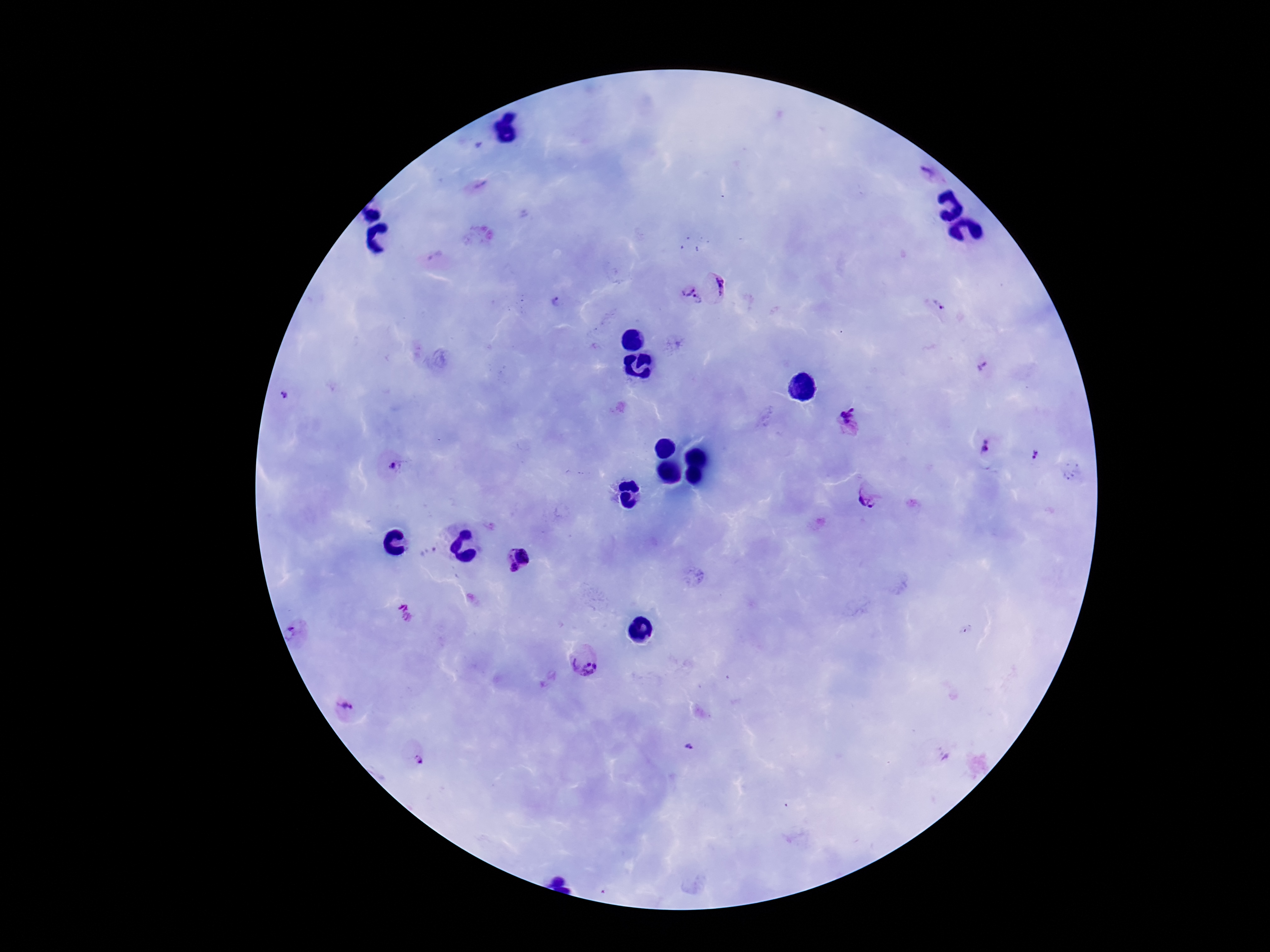
magnification = 100x
image size = 1270×952 pixels
capture = smartphone camera through the microscope eyepiece
preparation = thick peripheral-blood smear
field of view = one from this slide
Plasmodium parasite locations = approximate object centers, in pixels from the top-left corner: (x=928, y=173), (x=476, y=188), (x=717, y=286), (x=691, y=298), (x=555, y=302), (x=938, y=305), (x=983, y=367), (x=284, y=395), (x=850, y=423), (x=986, y=445), (x=1035, y=454), (x=390, y=465), (x=1070, y=472), (x=869, y=495), (x=430, y=554), (x=518, y=558), (x=404, y=614), (x=295, y=632), (x=584, y=660), (x=348, y=707), (x=688, y=745), (x=416, y=758)
stain = Giemsa
patient malaria status = positive